Classify this cell by malaria status.
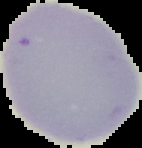
It is uninfected.

image_size: 142×148 pixels
preparation: thin blood film
image_type: segmented cell region with the area outside set to black